Report the malaria status.
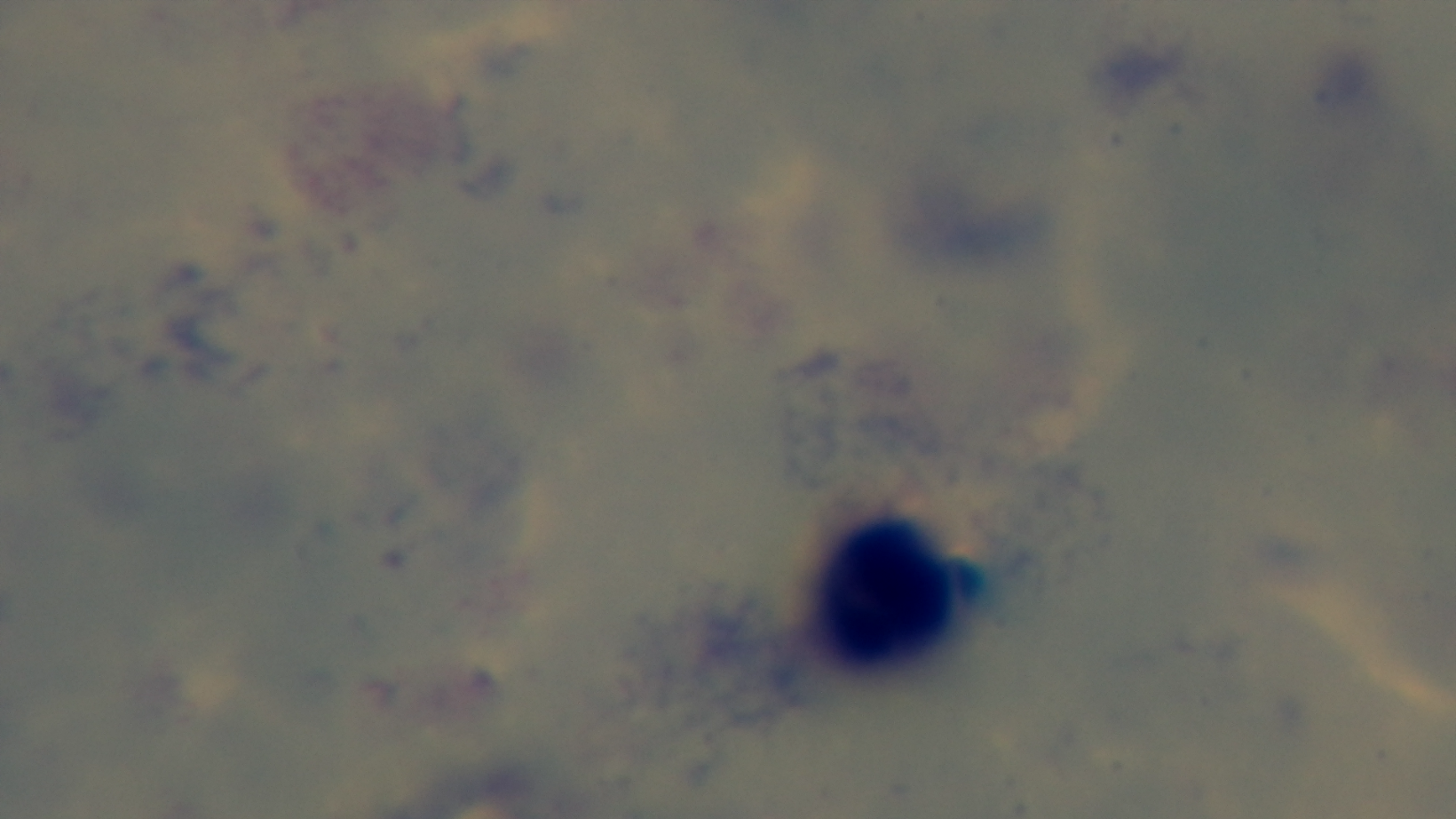
It is uninfected.

Summary:
  - Objective: 100x oil immersion
  - Field of view: one from the slide
  - Modality: light microscopy
  - Preparation: thick blood film
  - Capture: mounted 4K digital camera
  - Stain: Giemsa